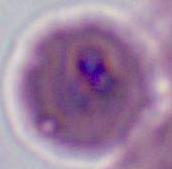
{
  "modality": "photomicrograph",
  "identification": "Plasmodium",
  "magnification": "400x or 1000x"
}